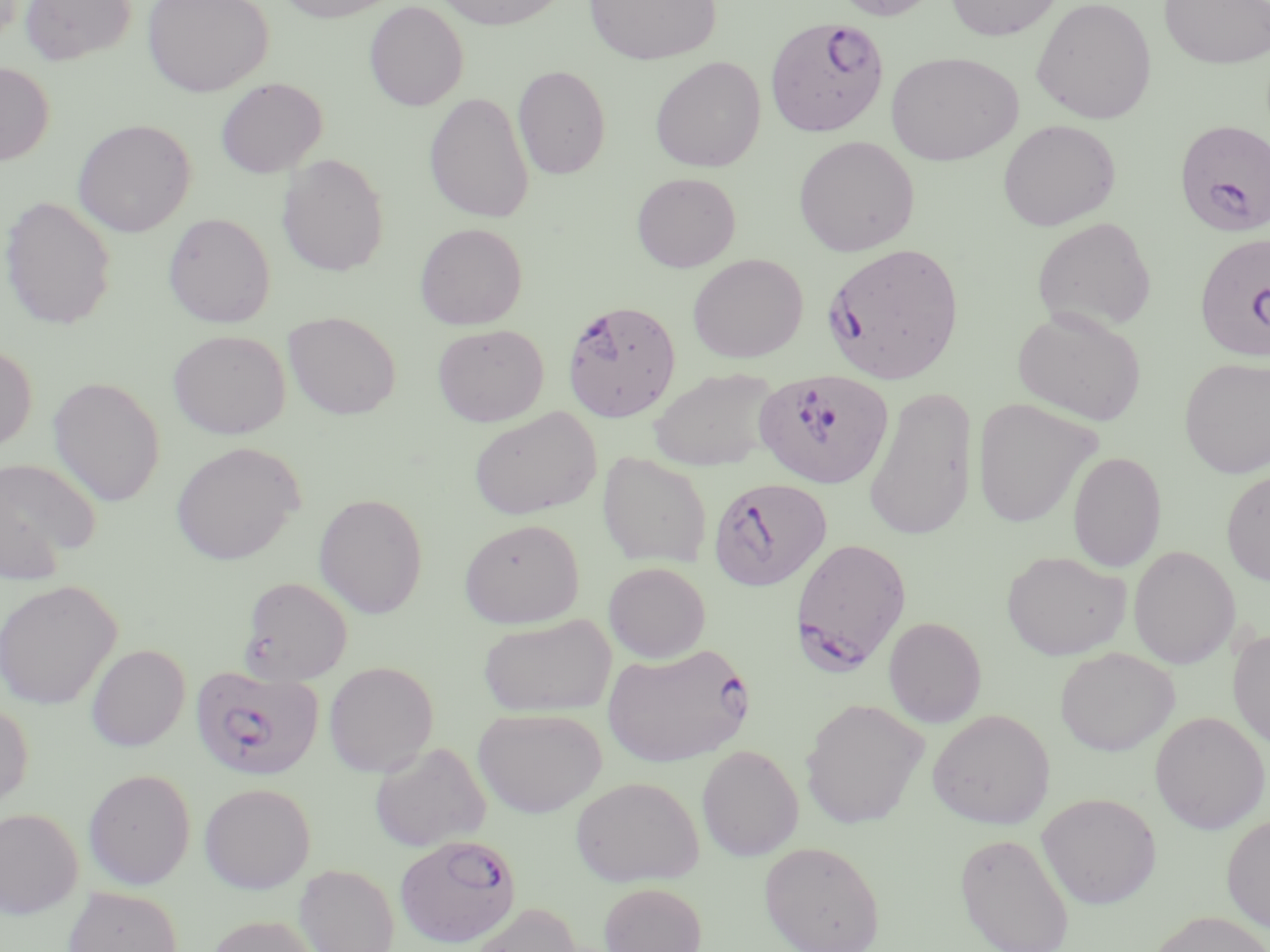 Approximate bounding boxes as (x1,y1)-(x2,y2) corner pairs in pixels. Plasmodium falciparum-infected red blood cell locations (subset): (766,15)-(890,137), (1175,119)-(1270,237), (1194,232)-(1270,364), (821,242)-(965,385), (562,299)-(681,422), (753,373)-(893,488), (791,537)-(912,670), (602,643)-(753,767), (191,664)-(324,782), (394,834)-(521,947). Uninfected red blood cell locations (subset): (20,0)-(136,65), (143,0)-(273,96), (275,0)-(401,23), (433,0)-(569,30), (583,0)-(722,65), (826,0)-(943,21), (944,0)-(1063,40), (1031,0)-(1157,123), (1158,0)-(1270,70), (364,1)-(469,111), (886,51)-(1023,165), (650,56)-(766,172), (0,62)-(54,165), (513,65)-(611,180), (215,77)-(328,178), (424,92)-(535,224), (72,119)-(196,237), (998,119)-(1121,230), (793,135)-(919,256), (277,154)-(389,277), (632,172)-(741,272), (0,195)-(117,330), (164,213)-(275,328), (1031,216)-(1157,334), (415,222)-(528,329), (687,253)-(808,363), (1012,307)-(1146,426), (283,311)-(401,419), (432,323)-(550,426), (168,330)-(290,439), (0,343)-(37,453), (1179,356)-(1270,479), (648,367)-(782,471), (48,377)-(165,507), (863,387)-(978,542), (971,398)-(1099,529), (468,407)-(602,520), (171,441)-(305,565), (1067,451)-(1167,572), (597,452)-(713,568), (0,457)-(100,577), (1221,467)-(1270,585), (314,493)-(428,618), (458,519)-(585,627), (1128,545)-(1240,669), (1002,550)-(1131,660), (603,561)-(711,663), (239,576)-(353,684), (0,579)-(122,709), (478,614)-(616,718), (883,616)-(987,727), (1228,627)-(1270,750), (86,644)-(190,751), (1055,647)-(1180,756), (323,661)-(439,777), (800,698)-(929,829), (0,701)-(33,809), (473,707)-(607,818), (927,709)-(1055,829), (1149,711)-(1269,834), (370,742)-(491,852), (697,744)-(803,861), (83,769)-(196,889), (570,775)-(704,887), (199,782)-(316,893), (1037,792)-(1162,909), (0,807)-(84,918), (1221,812)-(1270,932), (954,831)-(1076,952), (759,840)-(885,952), (294,863)-(399,952), (599,881)-(707,952), (63,886)-(183,952), (467,902)-(583,952), (1146,910)-(1270,952), (205,914)-(325,952). Slide-level diagnosis: Plasmodium falciparum. Image is 1270×952 pixels. 1000x magnification. One field of a larger specimen. May-Grünwald-Giemsa stain. Thin blood smear. Light microscopy.